Classify this cell by malaria status.
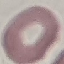

It is uninfected.

Cell patch, automatically extracted from a larger field of view and resized to 64 × 64 pixels. Thin blood film. Giemsa-stained preparation. Photographed with a smartphone camera at the microscope eyepiece.